Identify the parasite.
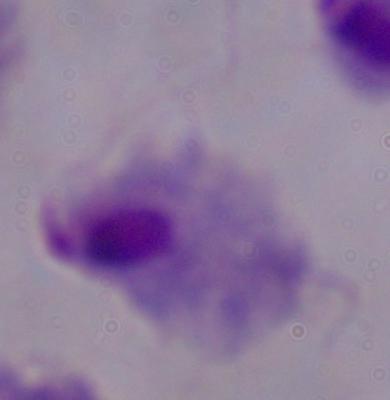
A trichomonad.

Summary:
  - Modality: micrograph
  - Magnification: 1000x